Draw a bounding box around every Plasmodium parasite, every leukocyte, and every artifact (stain precipitate or debris).
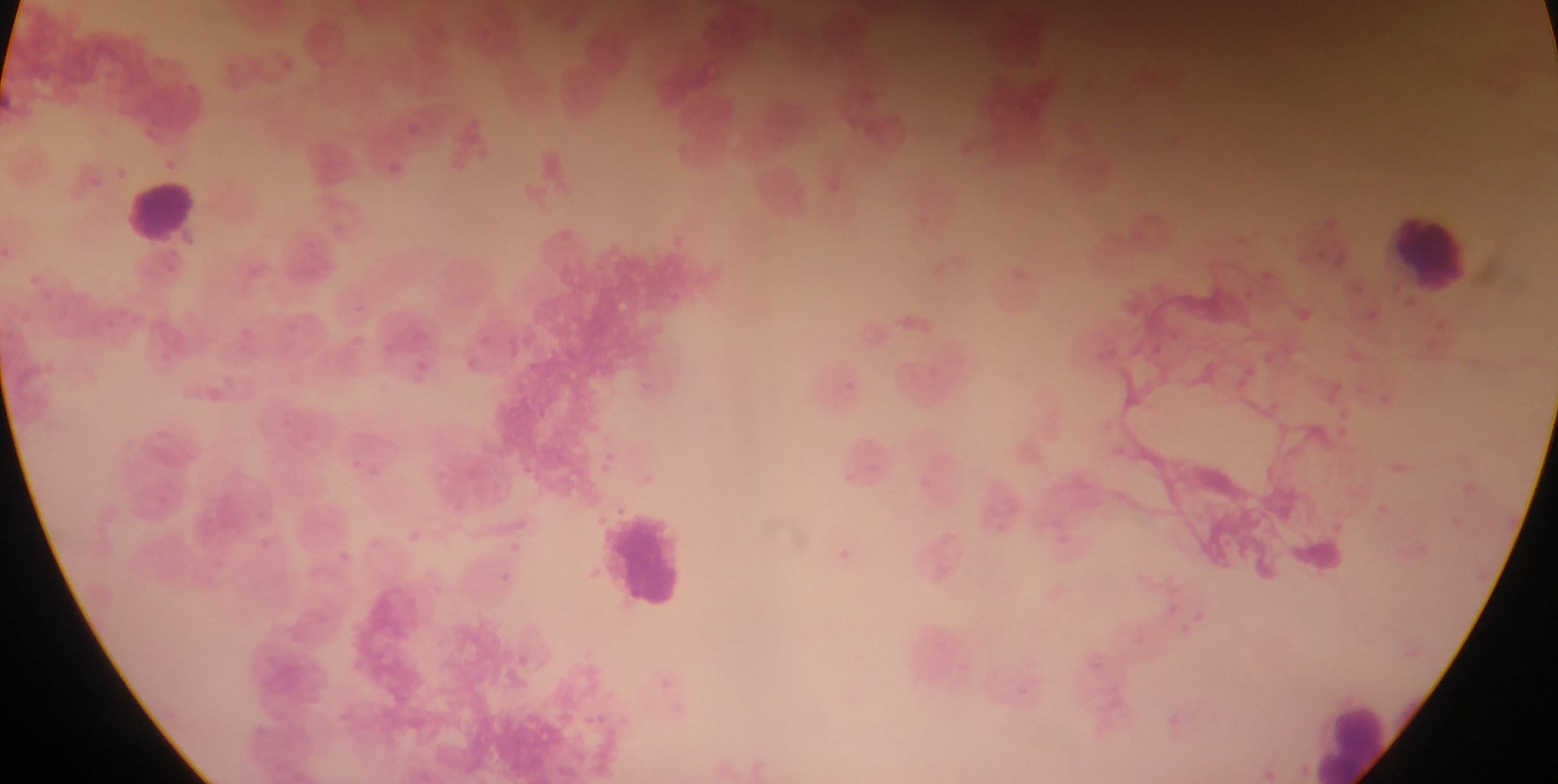
Approximate bounding boxes as left top right bottom in pixels.
Plasmodium parasites: 387 162 412 188; 349 331 369 351; 411 353 436 387; 195 379 233 413; 401 526 425 548; 391 527 431 557; 503 537 525 556; 834 537 863 574; 494 568 516 589.
Leukocytes: 118 173 205 248; 1386 213 1477 295; 602 510 696 614; 1305 689 1404 784.

Summary:
  - Field of view: single
  - Image size: 1558×784 pixels
  - Preparation: thin blood smear
  - Capture: mobile-phone photograph through a microscope
  - Country: Ghana